Report the malaria status of this cell.
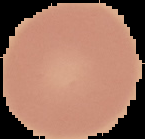
It is uninfected.

Summary:
  - Image type: cell region segmented out of the field of view; surrounding area masked to black
  - Preparation: thin blood smear
  - Image size: 145×139 pixels